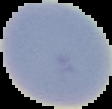

malaria status = uninfected
image type = segmented cell region on a black background
preparation = thin blood smear
image size = 112×109 pixels